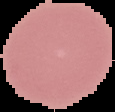

Image is 115×112 pixels. Malaria status: uninfected. Segmented cell region on a black background. From a thin blood smear.